Locate and identify every blood parasite.
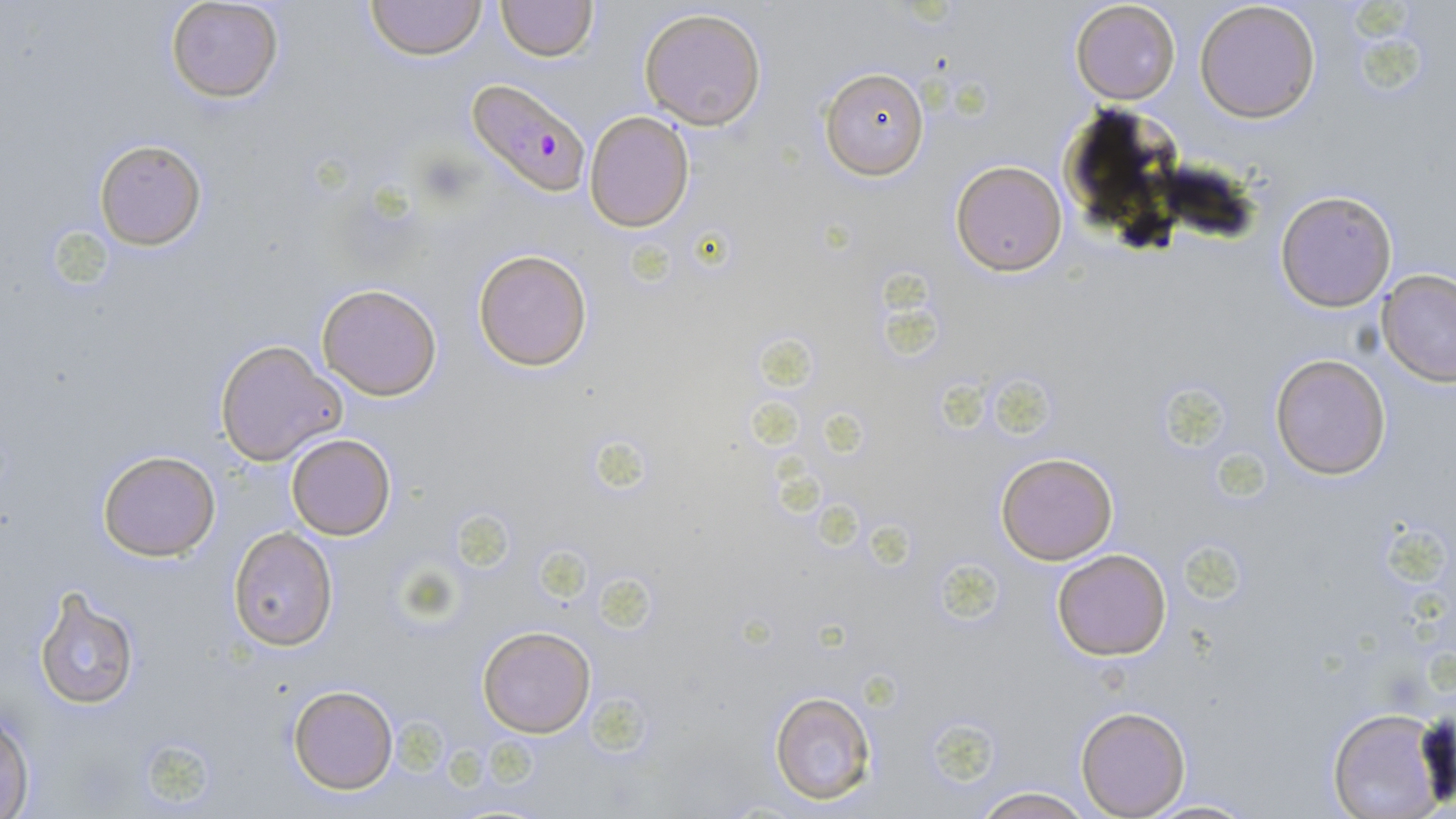

Approximate bounding boxes as [x1, y1, x2, y2] in pixels.
Plasmodium falciparum-infected red blood cells: [466, 78, 590, 197].
No Plasmodium ovale, Plasmodium malariae, Plasmodium vivax, Babesia divergens, or Trypanosoma brucei observed.

{
  "slide_level_diagnosis": "Plasmodium falciparum",
  "modality": "light microscopy",
  "image_size": "1456×819 pixels",
  "uninfected_red_blood_cell_locations": "approximate bounding boxes as [x1, y1, x2, y2] in pixels: [366, 0, 487, 61], [496, 0, 597, 60], [165, 1, 286, 104], [1070, 1, 1181, 105], [1195, 1, 1322, 123], [638, 7, 768, 129], [819, 66, 930, 181], [584, 110, 696, 233], [92, 138, 208, 250], [950, 161, 1067, 275], [1275, 189, 1398, 312], [473, 247, 594, 372], [1376, 270, 1456, 385], [317, 282, 443, 401], [216, 341, 345, 465], [1270, 353, 1392, 478], [285, 432, 397, 541], [96, 450, 220, 560], [996, 453, 1118, 565], [229, 527, 336, 649], [1050, 548, 1172, 661], [31, 587, 141, 710], [478, 625, 596, 737], [288, 684, 397, 793], [770, 690, 878, 805], [1327, 706, 1446, 819], [1076, 707, 1189, 817], [0, 709, 35, 817], [968, 785, 1096, 819], [1141, 796, 1256, 817]",
  "preparation": "thin blood smear",
  "stain": "May-Grünwald-Giemsa",
  "field_of_view": "one of a larger specimen",
  "magnification": "1000x"
}